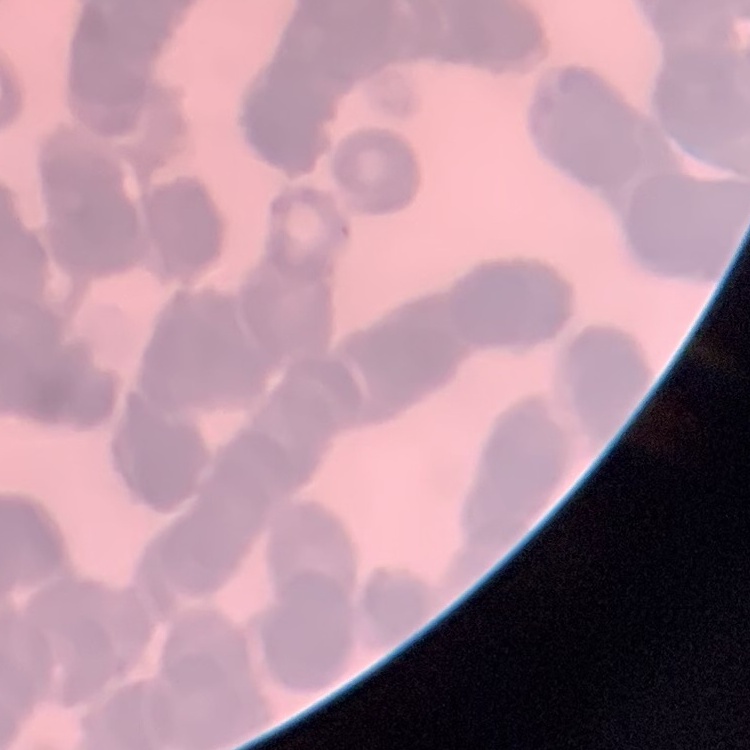

Summary:
  - Red blood cell morphology: rouleaux formation
  - Image type: square crop of a larger photomicrograph
  - Preparation: thin blood film
  - Stain: Field's or Giemsa